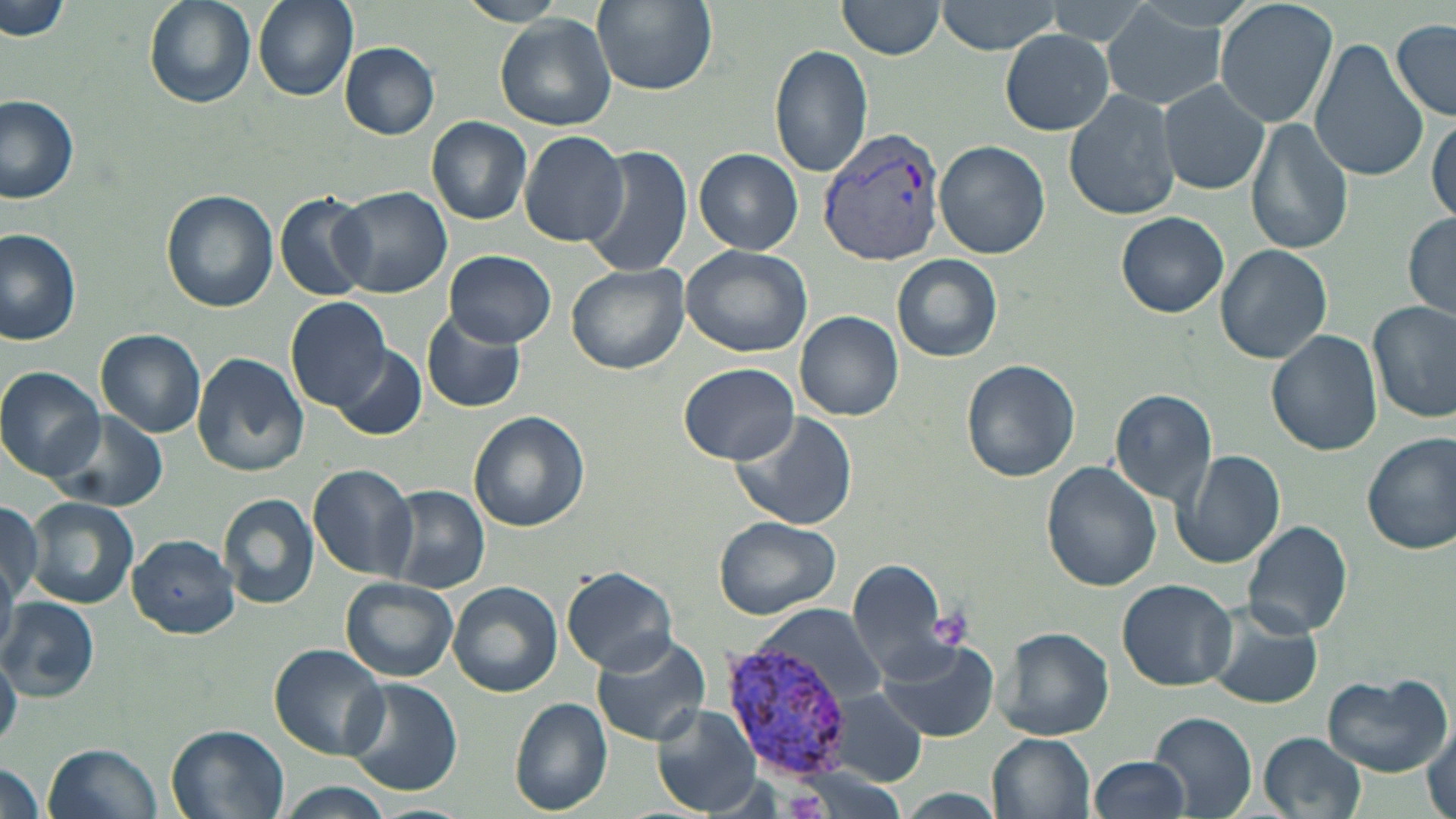
Approximate bounding boxes as (x1, y1, x2, y2) in pixels. Uninfected red blood cell locations: (253, 0, 357, 101), (453, 0, 569, 26), (838, 0, 947, 58), (934, 0, 1065, 55), (1212, 0, 1339, 130), (2, 1, 71, 41), (144, 1, 256, 109), (591, 1, 717, 95), (1100, 2, 1233, 109), (494, 14, 617, 131), (1392, 20, 1456, 121), (999, 31, 1116, 135), (1309, 39, 1428, 183), (339, 42, 440, 140), (771, 43, 874, 179), (1159, 79, 1270, 194), (1064, 87, 1179, 221), (0, 95, 80, 204), (1428, 115, 1456, 221), (426, 116, 533, 224), (1247, 117, 1354, 256), (518, 131, 627, 247), (935, 141, 1049, 257), (579, 144, 692, 278), (696, 148, 803, 253), (332, 184, 452, 297), (160, 189, 280, 313), (275, 191, 375, 300), (1115, 211, 1230, 318), (1403, 213, 1456, 319), (0, 229, 81, 345), (1213, 245, 1333, 364), (681, 246, 813, 357), (444, 250, 556, 347), (891, 254, 1003, 363), (565, 263, 691, 376), (286, 297, 392, 412), (1368, 301, 1456, 422), (421, 309, 527, 414), (794, 312, 903, 420), (1294, 312, 1429, 438), (1266, 329, 1382, 456), (97, 330, 206, 436), (331, 342, 426, 440), (191, 351, 310, 478), (961, 359, 1081, 483), (679, 363, 799, 464), (1, 366, 105, 479), (1109, 388, 1217, 507), (51, 409, 170, 513), (728, 409, 858, 533), (470, 412, 590, 533), (1362, 434, 1456, 555), (1174, 449, 1285, 571), (1041, 462, 1160, 592), (307, 463, 419, 581), (380, 485, 490, 595), (218, 493, 320, 610), (23, 497, 139, 610), (0, 501, 43, 603), (712, 515, 840, 619), (1242, 519, 1354, 639), (127, 533, 241, 639), (846, 559, 955, 679), (560, 567, 681, 675), (339, 578, 460, 682), (1115, 579, 1238, 690), (448, 581, 563, 696), (0, 595, 99, 699), (758, 607, 887, 710), (1208, 609, 1323, 709), (996, 627, 1114, 740), (588, 633, 711, 747), (874, 638, 999, 742), (269, 643, 389, 760), (0, 652, 21, 749), (1321, 671, 1452, 776), (339, 679, 461, 797), (829, 690, 931, 786), (510, 698, 614, 815), (651, 704, 765, 815), (1147, 710, 1257, 818), (1425, 725, 1455, 819), (165, 726, 290, 819), (1258, 732, 1367, 818), (989, 733, 1096, 817), (45, 742, 159, 819), (1090, 756, 1191, 818), (0, 761, 45, 819), (274, 782, 397, 819), (893, 789, 1006, 818), (365, 803, 478, 819). Platelet locations: (930, 609, 971, 650). Plasmodium vivax-infected red blood cell locations: (819, 129, 946, 265), (720, 638, 858, 784). Slide-level diagnosis: Plasmodium vivax. Captured at 1000x magnification. Light microscopy. Image is 1456×819 pixels. Single field of view. Thin blood film. May-Grünwald-Giemsa stain.